Name the parasite shown.
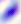
This is Toxoplasma gondii.

Micrograph. Captured at 400x magnification.